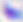
Micrograph. 400x magnification. Toxoplasma gondii is seen.